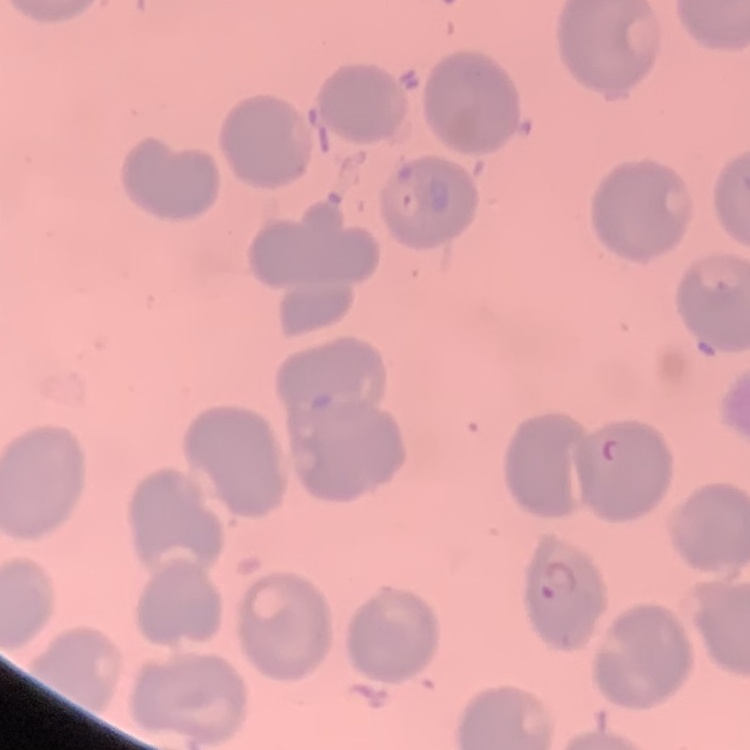

Summary:
  - Red blood cell morphology: no rouleaux formation
  - Stain: Field's or Giemsa
  - Image type: one tile cut from a larger photomicrograph
  - Preparation: thin blood film